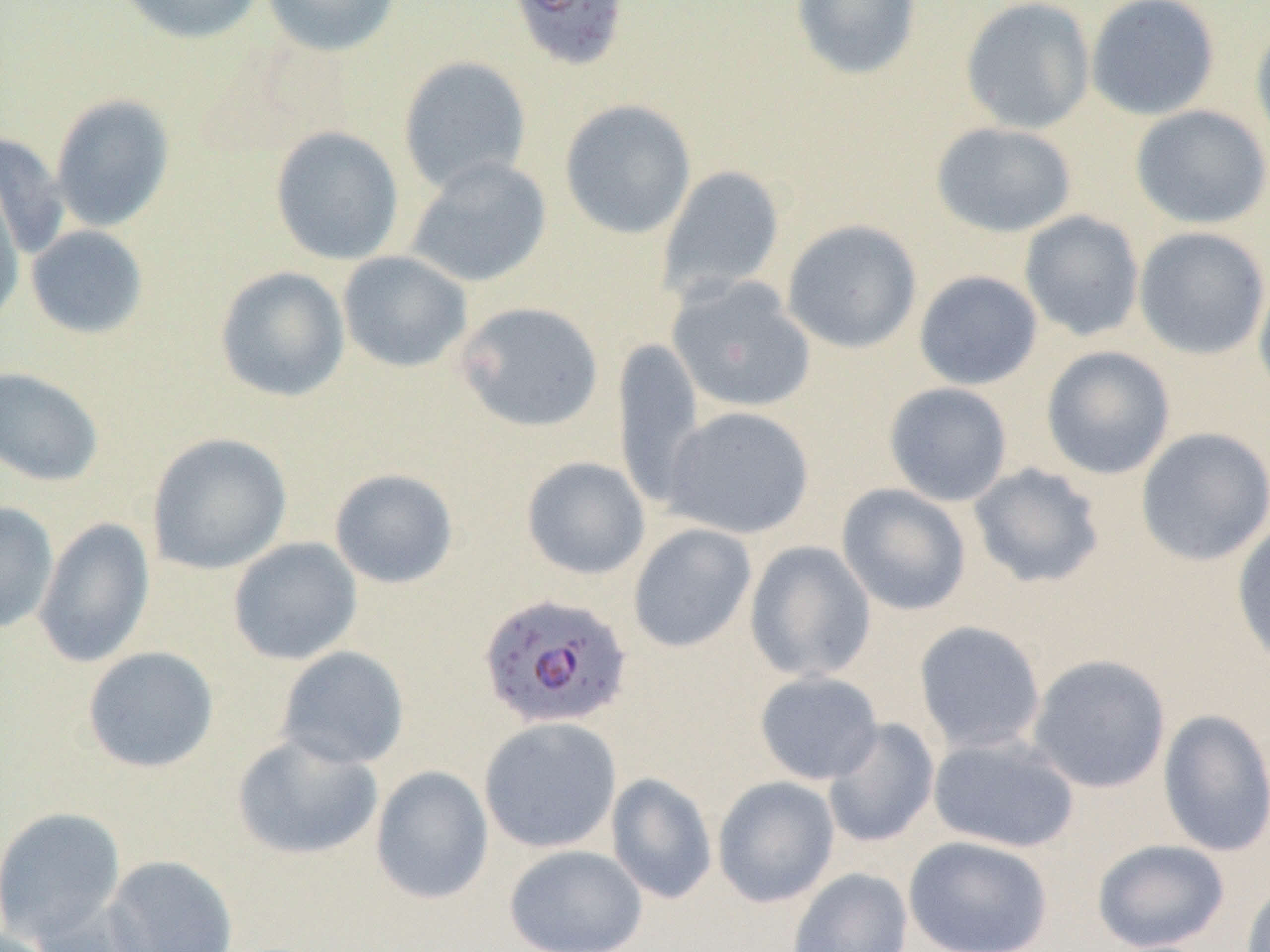 Approximate bounding boxes as (x1, y1, x2, y2) in pixels. Plasmodium falciparum-infected red blood cell locations: (507, 0, 632, 74), (479, 592, 632, 731). Uninfected red blood cell locations: (112, 0, 266, 45), (261, 0, 403, 57), (790, 0, 922, 80), (960, 0, 1096, 135), (1085, 0, 1221, 121), (1250, 18, 1270, 151), (398, 55, 532, 194), (50, 94, 175, 232), (559, 99, 697, 239), (1130, 105, 1270, 229), (930, 122, 1079, 238), (269, 125, 404, 265), (0, 133, 69, 260), (405, 156, 552, 288), (656, 164, 785, 301), (0, 182, 25, 328), (1019, 210, 1145, 341), (781, 219, 922, 354), (25, 225, 149, 339), (1133, 226, 1270, 360), (337, 251, 472, 373), (214, 265, 350, 403), (1253, 270, 1270, 406), (913, 271, 1043, 390), (666, 277, 816, 413), (455, 301, 604, 433), (612, 338, 705, 508), (1040, 345, 1176, 480), (0, 366, 104, 487), (883, 382, 1013, 507), (663, 406, 815, 539), (1135, 426, 1270, 567), (146, 432, 292, 575), (521, 456, 650, 580), (968, 463, 1105, 589), (328, 467, 459, 589), (836, 483, 972, 616), (0, 501, 58, 634), (33, 517, 156, 668), (1231, 519, 1270, 669), (627, 522, 757, 653), (228, 537, 362, 665), (744, 540, 876, 683), (913, 620, 1046, 754), (82, 646, 219, 773), (276, 646, 409, 770), (1027, 654, 1171, 793), (754, 671, 884, 785), (1157, 708, 1270, 857), (479, 716, 623, 853), (822, 718, 940, 849), (232, 732, 383, 860), (928, 734, 1080, 854), (370, 765, 494, 904), (606, 772, 717, 904), (712, 776, 840, 908), (0, 806, 127, 945), (903, 835, 1053, 952), (1092, 839, 1231, 951), (504, 844, 648, 952), (104, 855, 238, 952), (786, 867, 913, 952), (1241, 877, 1270, 952), (29, 898, 155, 952). Slide-level diagnosis: Plasmodium falciparum. Optical microscopy. Thin blood smear. Single field of view. 1000x magnification. Image is 1270×952 pixels.